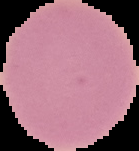
The area outside the segmented cell region is set to black. From a thin blood smear. Result: negative for Plasmodium parasites. Image is 139×151 pixels.